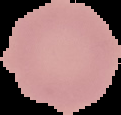

Malaria status: uninfected. From a thin blood film. Image is 121×115 pixels. Cell region segmented out of the field of view; the surrounding area is masked to black.